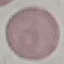
{
  "result": "no malaria parasites seen",
  "capture": "smartphone through the microscope eyepiece",
  "stain": "Giemsa",
  "image_type": "automatically extracted cell patch, resized to 64 × 64 pixels",
  "preparation": "thin smear"
}